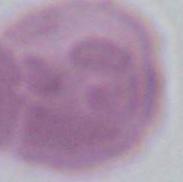
Summary:
  - Magnification: 1000x
  - Identification: erythrocyte
  - Modality: micrograph